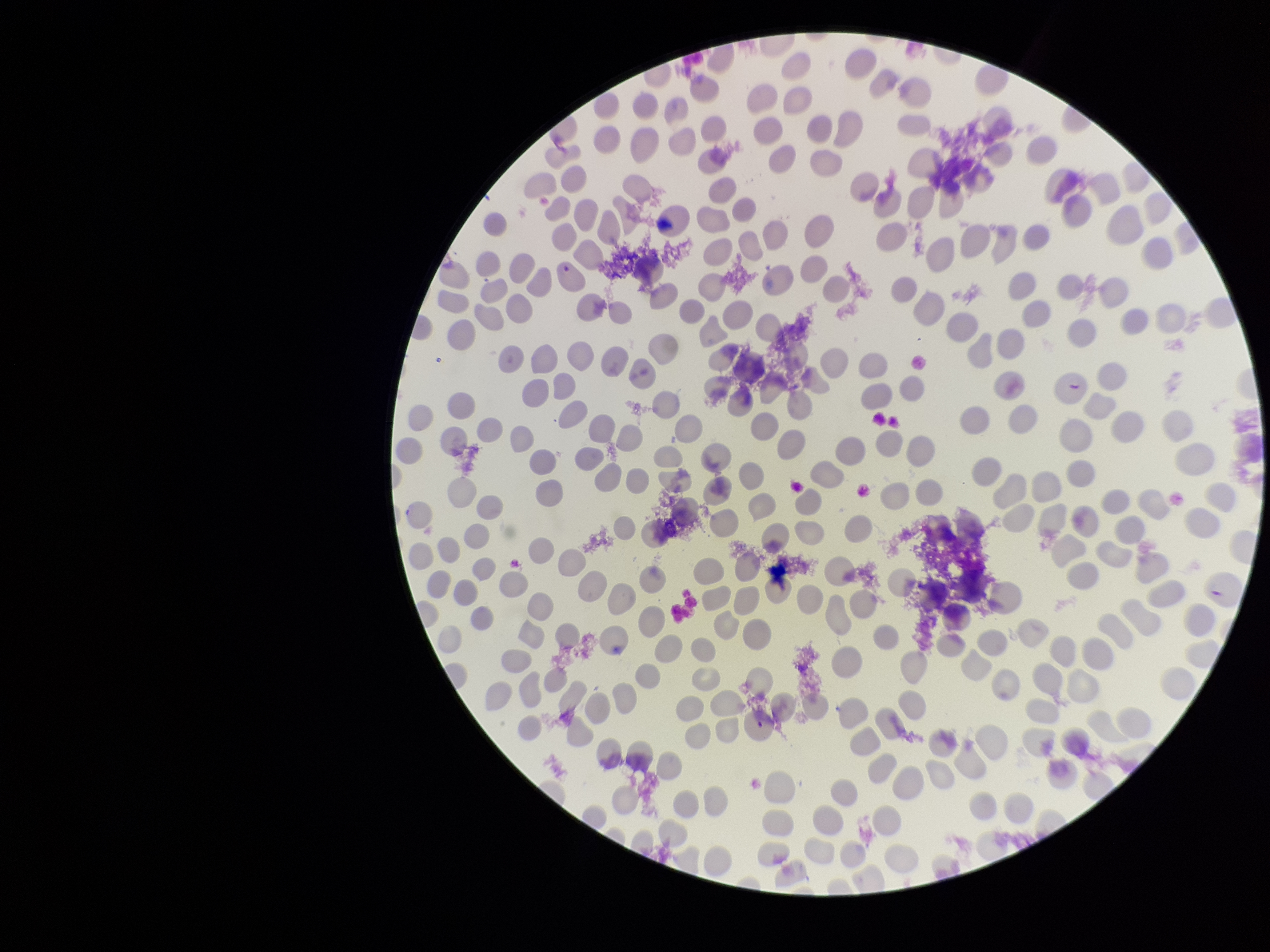

Summary:
  - Species reported for this patient: Plasmodium falciparum
  - Capture: smartphone photograph through the microscope eyepiece
  - Image size: 1270×952 pixels
  - Preparation: thin
  - Stain: Giemsa
  - Red blood cell count: 267
  - Field of view: single
  - Patient malaria status: infected
  - Parasitized red blood cells: seen
  - Parasitized red blood cell count: 3